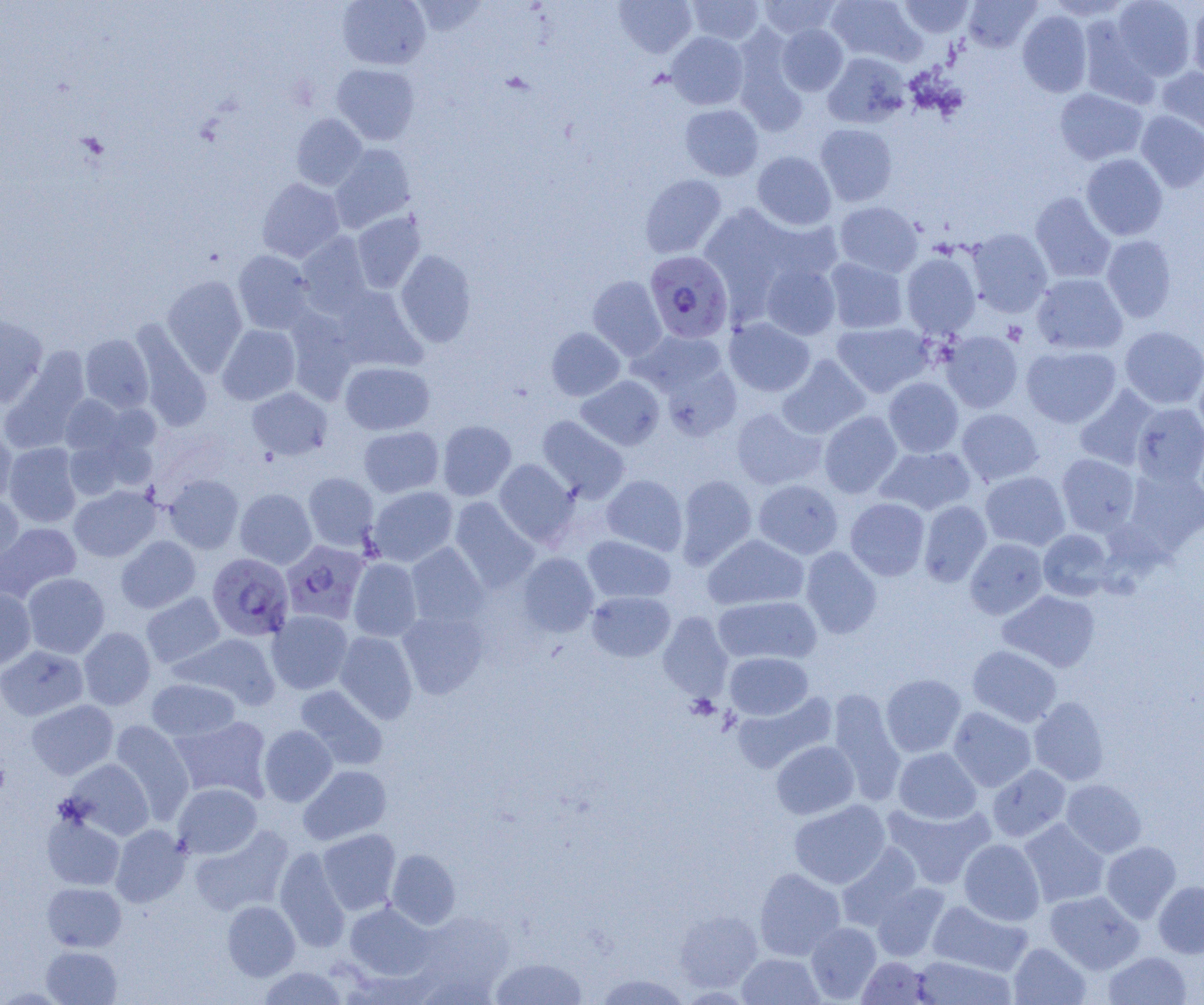
slide-level diagnosis = Plasmodium falciparum
preparation = thin blood smear
modality = light microscopy
Plasmodium falciparum-infected red blood cell locations = approximate bounding boxes as (x1, y1, x2, y2) in pixels: (645, 250, 734, 343), (281, 540, 369, 625), (207, 553, 294, 641)
platelet locations = approximate bounding boxes as (x1, y1, x2, y2) in pixels: (1003, 321, 1027, 345)
image size = 1204×1005 pixels
magnification = 1000x
uninfected red blood cell locations = approximate bounding boxes as (x1, y1, x2, y2) in pixels: (337, 0, 431, 70), (614, 0, 697, 58), (687, 0, 765, 45), (758, 0, 842, 39), (826, 0, 925, 66), (898, 0, 974, 38), (963, 0, 1041, 52), (1045, 0, 1133, 21), (1111, 0, 1196, 82), (1187, 4, 1204, 84), (1017, 10, 1092, 97), (1077, 15, 1159, 106), (776, 23, 848, 95), (732, 30, 809, 134), (666, 32, 749, 110), (822, 52, 910, 128), (332, 64, 420, 145), (1157, 66, 1204, 140), (1054, 88, 1148, 165), (679, 104, 763, 181), (1135, 111, 1204, 192), (291, 113, 367, 190), (815, 123, 898, 207), (330, 144, 416, 232), (752, 151, 836, 230), (1080, 153, 1168, 241), (640, 174, 727, 258), (257, 178, 345, 263), (1030, 192, 1116, 284), (834, 201, 923, 277), (698, 204, 799, 310), (352, 212, 426, 293), (757, 214, 844, 284), (967, 228, 1053, 317), (296, 232, 373, 316), (1101, 235, 1177, 323), (232, 250, 315, 334), (396, 250, 476, 348), (901, 252, 981, 338), (824, 256, 908, 334), (760, 262, 841, 339), (1031, 273, 1127, 355), (161, 275, 247, 375), (588, 276, 667, 361), (331, 286, 425, 372), (284, 309, 359, 403), (0, 315, 48, 407), (724, 317, 815, 397), (131, 320, 212, 431), (832, 321, 934, 398), (217, 324, 300, 405), (1120, 326, 1204, 409), (546, 327, 625, 401), (632, 329, 727, 397), (940, 331, 1023, 413), (80, 334, 154, 413), (1021, 345, 1121, 428), (1, 351, 90, 452), (778, 355, 870, 439), (1194, 360, 1204, 446), (340, 361, 435, 435), (661, 363, 742, 441), (576, 375, 664, 450), (883, 377, 964, 457), (1074, 385, 1160, 471), (247, 387, 332, 460), (59, 395, 130, 457), (1131, 402, 1204, 486), (731, 406, 826, 490), (957, 408, 1044, 486), (819, 410, 902, 498), (537, 415, 630, 502), (437, 420, 516, 500), (358, 426, 443, 497), (0, 429, 17, 505), (63, 434, 139, 501), (3, 442, 82, 527), (875, 446, 976, 516), (1057, 453, 1140, 536), (494, 459, 578, 547), (1123, 466, 1204, 554), (980, 471, 1070, 551), (303, 472, 379, 551), (164, 474, 243, 553), (676, 474, 757, 569), (602, 475, 688, 555), (753, 479, 843, 559), (69, 485, 160, 562), (367, 486, 458, 567), (235, 488, 317, 569), (0, 493, 23, 575), (450, 496, 539, 592), (845, 498, 930, 580), (919, 500, 992, 586), (0, 522, 81, 602), (1038, 529, 1114, 600), (702, 534, 809, 610), (115, 535, 201, 613), (583, 535, 675, 603), (965, 538, 1048, 619), (405, 542, 489, 627), (800, 546, 882, 639), (517, 553, 598, 637), (348, 558, 422, 642), (22, 573, 109, 658), (0, 588, 36, 670), (587, 590, 675, 662), (998, 590, 1100, 672), (141, 592, 225, 670), (713, 595, 821, 665), (397, 607, 489, 699), (267, 610, 353, 694), (658, 612, 733, 700), (78, 627, 155, 710), (334, 631, 418, 723), (174, 632, 281, 710), (967, 644, 1062, 727), (0, 646, 88, 721), (725, 652, 814, 720), (881, 674, 966, 757), (146, 678, 240, 741), (295, 685, 388, 771), (828, 689, 907, 805), (732, 692, 837, 774), (1029, 696, 1109, 786), (27, 699, 118, 779), (948, 707, 1036, 792), (169, 715, 272, 802), (109, 720, 195, 823), (259, 725, 337, 806), (771, 741, 859, 819), (893, 747, 981, 824), (64, 758, 154, 840), (987, 764, 1071, 842), (299, 765, 391, 845), (1061, 779, 1147, 858), (173, 783, 262, 858), (789, 800, 890, 889), (882, 801, 995, 889), (41, 811, 125, 891), (1019, 819, 1110, 907), (111, 825, 190, 907), (190, 825, 294, 916), (318, 829, 401, 914), (959, 838, 1045, 925), (1101, 840, 1181, 923), (837, 844, 922, 931), (275, 846, 350, 951), (386, 849, 461, 929), (754, 868, 845, 960), (1154, 881, 1204, 957), (42, 882, 126, 951), (872, 882, 951, 961), (1044, 890, 1145, 974), (222, 900, 300, 980), (928, 900, 1032, 976), (345, 902, 434, 981), (675, 910, 762, 993), (805, 922, 881, 1003), (1009, 942, 1091, 1005), (41, 945, 122, 1004), (1103, 951, 1192, 1005), (737, 953, 824, 1005), (490, 956, 587, 1004), (857, 956, 934, 1004), (911, 956, 1016, 1004), (256, 965, 349, 1005), (594, 973, 693, 1005)
field of view = single